Assess this cell for malaria.
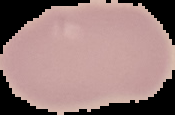

Uninfected.

Summary:
  - Preparation: thin blood film
  - Image type: segmented cell region with the area outside set to black
  - Image size: 175×115 pixels